Report the malaria status of this cell.
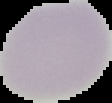

Uninfected.

preparation = thin blood film
image type = segmented cell region on a black background
image size = 112×103 pixels